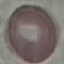
Summary:
  - Malaria status: uninfected
  - Preparation: thin blood film
  - Stain: Giemsa
  - Capture: smartphone camera at the microscope eyepiece
  - Image type: automatically extracted cell patch, resized to 64 × 64 pixels